Report the malaria status of this cell.
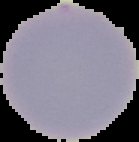

It is uninfected.

image_size: 139×142 pixels
image_type: segmented cell region on a black background
preparation: thin blood film